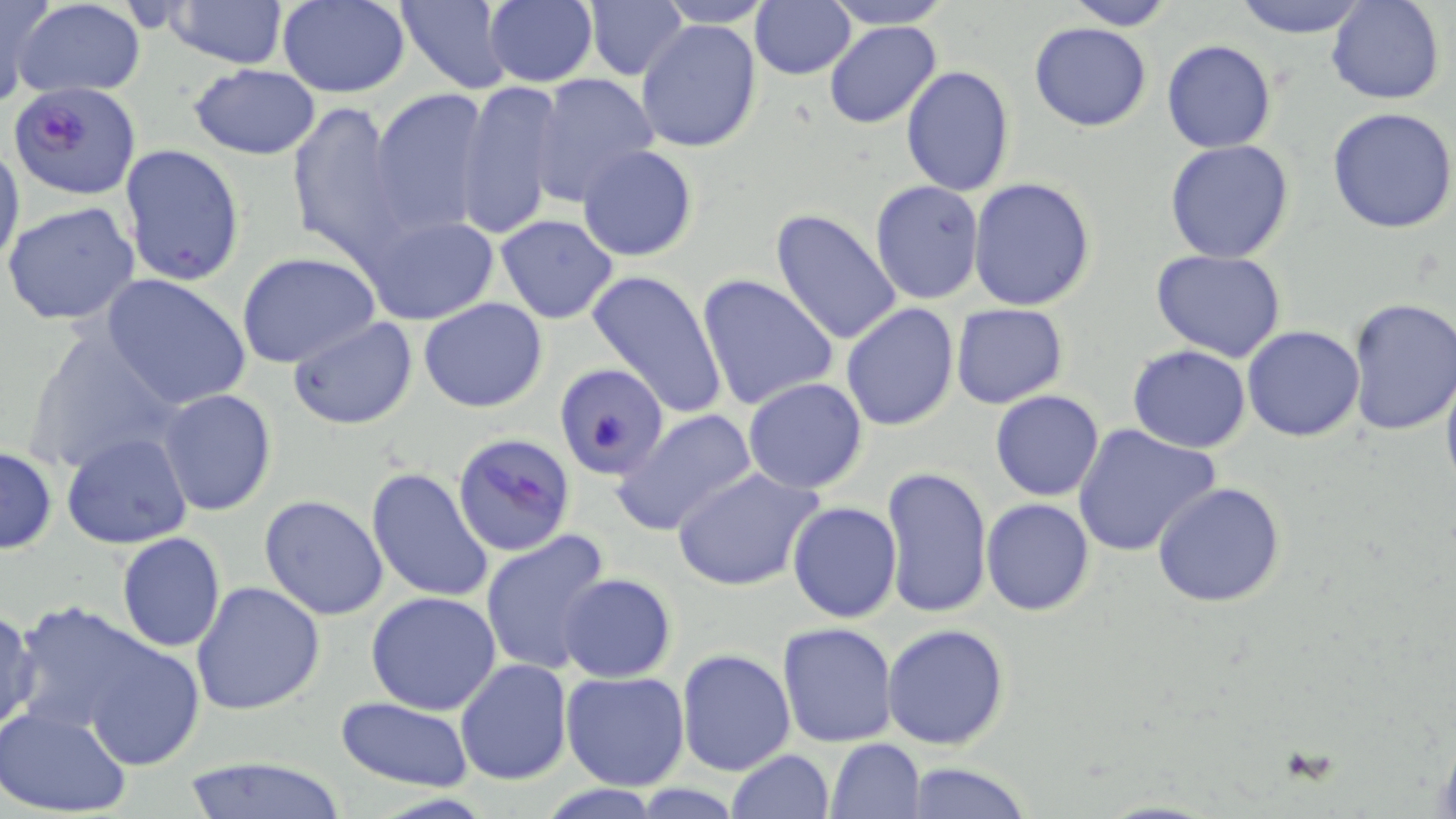

Approximate bounding boxes as named x1/y1/x2/y2 corners in pixels. Uninfected red blood cell locations: (x1=0, y1=0, x2=51, y2=109), (x1=165, y1=0, x2=289, y2=69), (x1=394, y1=0, x2=513, y2=92), (x1=482, y1=0, x2=598, y2=87), (x1=585, y1=0, x2=687, y2=82), (x1=821, y1=0, x2=953, y2=29), (x1=1061, y1=0, x2=1179, y2=29), (x1=1232, y1=0, x2=1370, y2=39), (x1=1327, y1=0, x2=1445, y2=105), (x1=13, y1=1, x2=147, y2=99), (x1=278, y1=1, x2=411, y2=97), (x1=652, y1=1, x2=777, y2=27), (x1=750, y1=1, x2=856, y2=80), (x1=823, y1=19, x2=942, y2=129), (x1=636, y1=20, x2=763, y2=154), (x1=1028, y1=22, x2=1152, y2=132), (x1=1161, y1=39, x2=1279, y2=153), (x1=188, y1=64, x2=323, y2=160), (x1=899, y1=66, x2=1015, y2=195), (x1=531, y1=72, x2=658, y2=205), (x1=454, y1=78, x2=566, y2=239), (x1=369, y1=89, x2=493, y2=234), (x1=287, y1=100, x2=408, y2=259), (x1=1328, y1=106, x2=1456, y2=232), (x1=0, y1=139, x2=25, y2=278), (x1=1165, y1=140, x2=1296, y2=263), (x1=119, y1=144, x2=245, y2=289), (x1=577, y1=144, x2=701, y2=262), (x1=969, y1=177, x2=1097, y2=311), (x1=870, y1=180, x2=984, y2=305), (x1=3, y1=201, x2=139, y2=328), (x1=769, y1=208, x2=903, y2=346), (x1=358, y1=210, x2=502, y2=326), (x1=493, y1=214, x2=619, y2=324), (x1=1149, y1=249, x2=1286, y2=362), (x1=238, y1=253, x2=381, y2=368), (x1=390, y1=258, x2=521, y2=398), (x1=585, y1=267, x2=729, y2=421), (x1=100, y1=272, x2=251, y2=410), (x1=695, y1=274, x2=842, y2=411), (x1=1345, y1=297, x2=1456, y2=436), (x1=418, y1=298, x2=548, y2=412), (x1=841, y1=302, x2=960, y2=432), (x1=951, y1=304, x2=1069, y2=408), (x1=288, y1=316, x2=419, y2=431), (x1=1242, y1=325, x2=1366, y2=441), (x1=21, y1=326, x2=184, y2=479), (x1=1126, y1=344, x2=1251, y2=453), (x1=553, y1=362, x2=667, y2=480), (x1=1441, y1=365, x2=1456, y2=495), (x1=742, y1=377, x2=869, y2=494), (x1=156, y1=388, x2=277, y2=516), (x1=989, y1=389, x2=1105, y2=501), (x1=612, y1=408, x2=759, y2=538), (x1=1071, y1=422, x2=1221, y2=558), (x1=62, y1=430, x2=192, y2=549), (x1=0, y1=445, x2=57, y2=553), (x1=672, y1=465, x2=824, y2=594), (x1=880, y1=466, x2=992, y2=619), (x1=366, y1=467, x2=495, y2=606), (x1=1152, y1=482, x2=1286, y2=607), (x1=258, y1=494, x2=390, y2=621), (x1=982, y1=498, x2=1095, y2=615), (x1=787, y1=501, x2=903, y2=623), (x1=479, y1=530, x2=615, y2=676), (x1=116, y1=532, x2=226, y2=653), (x1=556, y1=573, x2=677, y2=681), (x1=191, y1=581, x2=326, y2=717), (x1=366, y1=592, x2=503, y2=715), (x1=19, y1=601, x2=209, y2=765), (x1=0, y1=606, x2=41, y2=736), (x1=777, y1=622, x2=898, y2=749), (x1=882, y1=623, x2=1011, y2=750), (x1=676, y1=648, x2=796, y2=776), (x1=455, y1=659, x2=574, y2=785), (x1=562, y1=671, x2=690, y2=792), (x1=335, y1=698, x2=477, y2=792), (x1=0, y1=704, x2=135, y2=818), (x1=826, y1=738, x2=925, y2=818), (x1=724, y1=749, x2=833, y2=819), (x1=180, y1=755, x2=350, y2=819), (x1=902, y1=761, x2=1031, y2=819). Plasmodium falciparum-infected red blood cell locations: (x1=6, y1=81, x2=139, y2=200), (x1=453, y1=432, x2=576, y2=558). Slide-level diagnosis: Plasmodium falciparum. Thin blood film. Captured at 1000x magnification. Single field of view. Light microscopy. May-Grünwald-Giemsa stain. Image is 1456×819 pixels.